Report the malaria status of this cell.
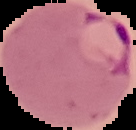

It is parasitized.

Summary:
  - Image size: 136×130 pixels
  - Preparation: thin blood film
  - Image type: segmented cell region with the area outside set to black